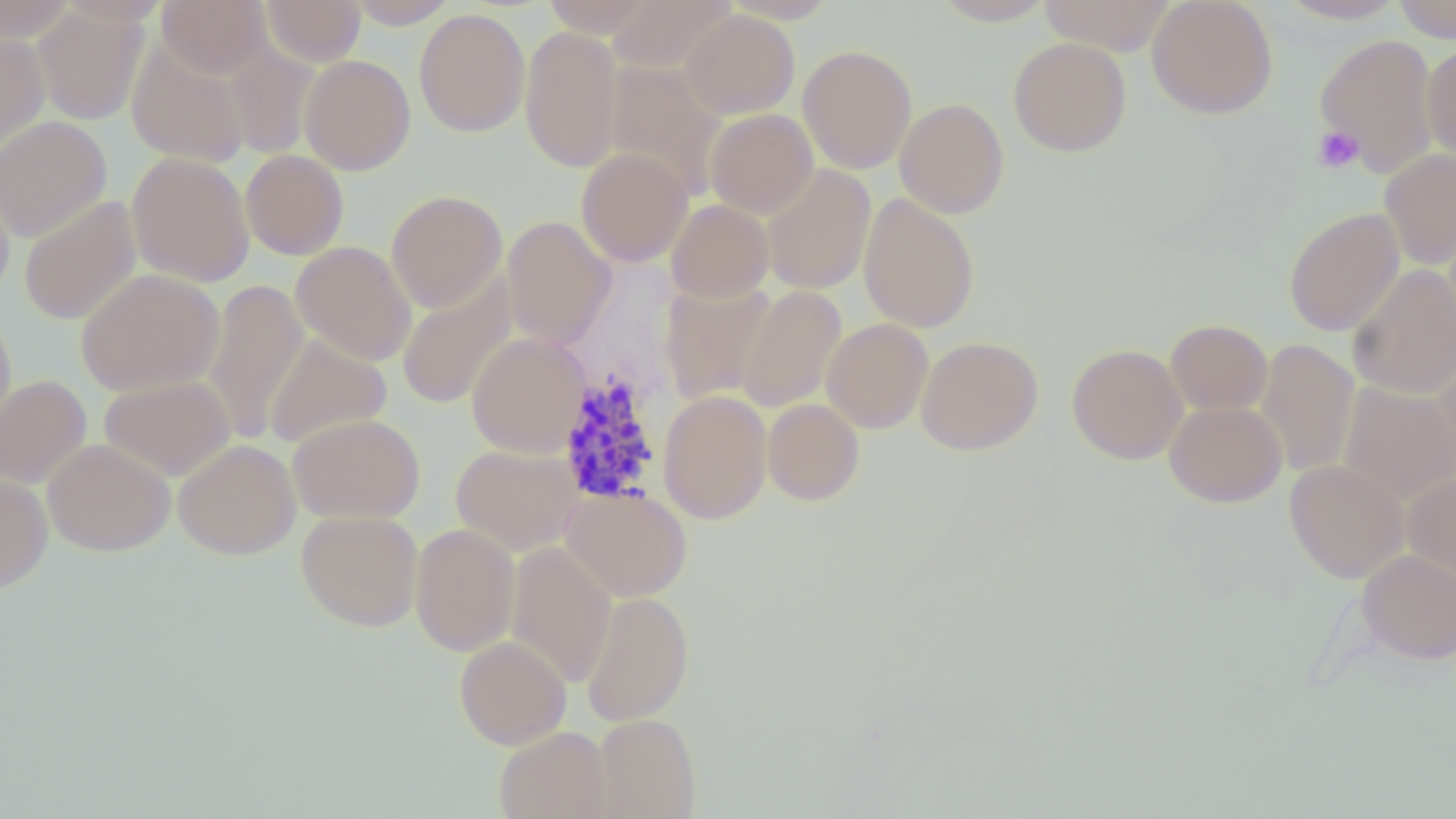
Approximate bounding boxes as (x1, y1, x2, y2) in pixels. Platelet locations: (1313, 126, 1364, 173). Plasmodium malariae-infected red blood cell locations: (557, 372, 664, 507). Uninfected red blood cell locations: (0, 0, 79, 42), (56, 0, 170, 29), (156, 0, 270, 77), (260, 0, 366, 66), (343, 0, 460, 28), (541, 0, 660, 37), (606, 0, 736, 75), (721, 0, 840, 24), (931, 0, 1056, 25), (1039, 0, 1176, 55), (1147, 0, 1278, 119), (1274, 0, 1410, 23), (1393, 0, 1455, 42), (32, 5, 150, 125), (413, 8, 530, 137), (680, 10, 800, 119), (519, 24, 623, 173), (0, 27, 50, 154), (1315, 33, 1439, 176), (126, 37, 252, 166), (1008, 37, 1132, 157), (223, 43, 320, 159), (1422, 44, 1456, 164), (798, 45, 918, 173), (300, 55, 416, 175), (604, 62, 728, 199), (895, 97, 1009, 218), (704, 108, 818, 218), (0, 115, 112, 242), (576, 148, 693, 266), (240, 149, 349, 260), (1379, 149, 1456, 268), (127, 151, 254, 287), (760, 163, 876, 295), (0, 177, 15, 307), (386, 190, 507, 313), (858, 192, 980, 333), (19, 194, 142, 326), (666, 199, 775, 303), (1283, 207, 1404, 336), (501, 215, 616, 350), (290, 241, 417, 366), (1347, 263, 1456, 399), (75, 268, 225, 396), (397, 277, 516, 410), (202, 278, 308, 444), (660, 280, 777, 405), (735, 285, 847, 413), (0, 309, 15, 437), (821, 318, 934, 433), (1166, 319, 1272, 415), (263, 332, 393, 450), (467, 332, 591, 458), (915, 336, 1043, 455), (1255, 339, 1360, 478), (1432, 339, 1456, 477), (1067, 343, 1188, 464), (0, 375, 92, 490), (99, 375, 235, 481), (1337, 381, 1456, 506), (658, 390, 773, 524), (762, 398, 864, 506), (1163, 400, 1287, 507), (288, 413, 425, 524), (42, 438, 175, 557), (173, 439, 301, 560), (450, 443, 583, 555), (1284, 459, 1409, 583), (1403, 471, 1456, 578), (0, 474, 53, 594), (561, 485, 692, 601), (296, 510, 424, 632), (409, 523, 521, 657), (505, 541, 617, 689), (1356, 550, 1456, 664), (580, 591, 695, 726), (454, 636, 571, 749), (592, 713, 701, 818), (494, 727, 612, 819). Slide-level diagnosis: Plasmodium malariae. One field of a larger specimen. Captured at 1000x magnification. Thin blood smear. Optical microscopy. Image is 1456×819 pixels. May-Grünwald-Giemsa stain.